Outline each uninfected red blood cell.
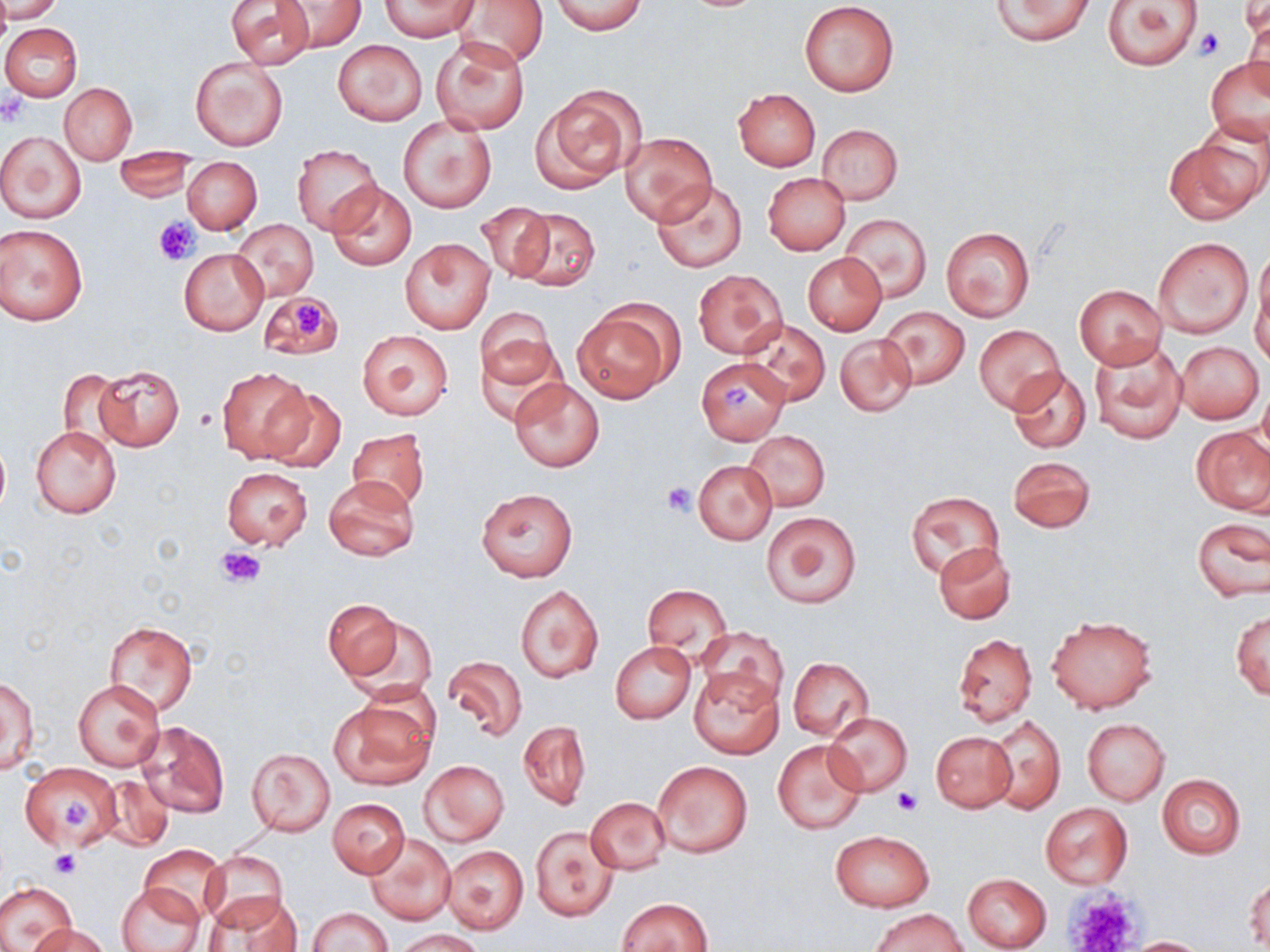
Approximate bounding boxes as (x1, y1, x2, y2) in pixels.
Uninfected red blood cells: (1, 0, 65, 23), (379, 0, 479, 40), (455, 0, 550, 69), (991, 0, 1094, 45), (1103, 0, 1203, 70), (227, 1, 315, 68), (277, 1, 366, 52), (799, 1, 901, 97), (551, 2, 648, 35), (1, 23, 82, 101), (433, 36, 531, 133), (334, 40, 426, 125), (190, 55, 289, 152), (1206, 57, 1270, 146), (61, 83, 136, 163), (538, 86, 644, 189), (733, 89, 821, 170), (398, 115, 497, 214), (818, 124, 902, 204), (0, 131, 87, 223), (622, 132, 716, 225), (1165, 137, 1263, 224), (292, 144, 382, 235), (114, 151, 197, 201), (183, 157, 262, 234), (763, 172, 849, 255), (652, 179, 746, 272), (326, 181, 416, 270), (477, 202, 555, 282), (512, 207, 601, 291), (841, 214, 931, 301), (232, 220, 319, 301), (0, 223, 89, 326), (941, 226, 1034, 322), (400, 237, 495, 333), (1153, 238, 1254, 337), (179, 247, 268, 335), (1252, 250, 1270, 361), (803, 252, 886, 335), (693, 269, 786, 357), (1073, 283, 1168, 370), (259, 291, 341, 359), (572, 304, 678, 402), (475, 308, 558, 393), (880, 308, 969, 389), (742, 319, 830, 406), (974, 325, 1064, 413), (357, 329, 454, 420), (835, 333, 917, 416), (1088, 341, 1186, 445), (1175, 341, 1264, 422), (696, 357, 790, 444), (92, 364, 185, 451), (217, 366, 313, 463), (1007, 368, 1091, 452), (57, 369, 128, 453), (509, 377, 604, 472), (262, 388, 344, 470), (31, 425, 121, 518), (1191, 426, 1269, 514), (346, 428, 430, 513), (744, 430, 830, 511), (0, 439, 10, 515), (1008, 455, 1096, 533), (692, 459, 777, 545), (222, 467, 312, 549), (323, 476, 418, 561), (475, 487, 578, 582), (906, 491, 1003, 577), (763, 510, 862, 609), (1192, 517, 1268, 602), (933, 542, 1016, 624), (515, 584, 604, 683), (642, 584, 731, 661), (324, 598, 403, 682), (1231, 610, 1269, 698), (338, 611, 435, 701), (1045, 613, 1158, 712), (105, 621, 199, 715), (699, 627, 789, 708), (953, 633, 1037, 725), (611, 641, 696, 723), (442, 655, 528, 741), (787, 657, 874, 740), (688, 666, 784, 758), (2, 674, 39, 776), (72, 680, 164, 771), (329, 697, 435, 789), (824, 712, 912, 796), (989, 713, 1065, 814), (1082, 718, 1169, 804), (134, 720, 230, 819), (517, 720, 591, 810), (930, 731, 1016, 812), (772, 738, 868, 836), (247, 748, 335, 836), (419, 760, 509, 846), (653, 760, 752, 858), (19, 763, 120, 850), (98, 774, 174, 851), (1156, 774, 1246, 858), (586, 797, 671, 874), (328, 798, 409, 878), (1039, 802, 1132, 889), (530, 826, 618, 923), (831, 830, 932, 911), (366, 833, 455, 925), (140, 845, 229, 923), (441, 845, 530, 936), (202, 851, 289, 930), (962, 871, 1053, 952), (1245, 875, 1269, 951), (0, 882, 75, 950), (117, 882, 206, 952), (201, 892, 303, 951), (616, 897, 712, 952), (308, 906, 393, 952), (872, 908, 967, 952), (28, 922, 110, 952), (395, 929, 485, 951), (1127, 936, 1211, 951).

Platelet locations: (1194, 26, 1224, 59), (0, 94, 26, 125), (154, 216, 200, 265), (285, 295, 325, 336), (723, 384, 751, 413), (662, 483, 696, 515), (216, 545, 266, 588), (891, 789, 919, 816), (62, 798, 91, 830), (49, 851, 80, 878), (1066, 890, 1144, 952). Slide-level diagnosis: no evidence of blood parasites. Thin blood film. Captured at 1000x magnification. One field of a larger specimen. Optical microscopy. May-Grünwald-Giemsa stain. Image is 1270×952 pixels.